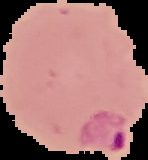

Summary:
  - Image size: 148×160 pixels
  - Preparation: thin blood smear
  - Result: Plasmodium parasites identified
  - Image type: segmented cell region on a black background